Name the parasite shown.
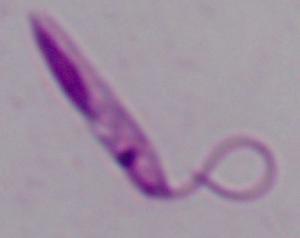
This is Leishmania.

Summary:
  - Magnification: 1000x
  - Modality: photomicrograph